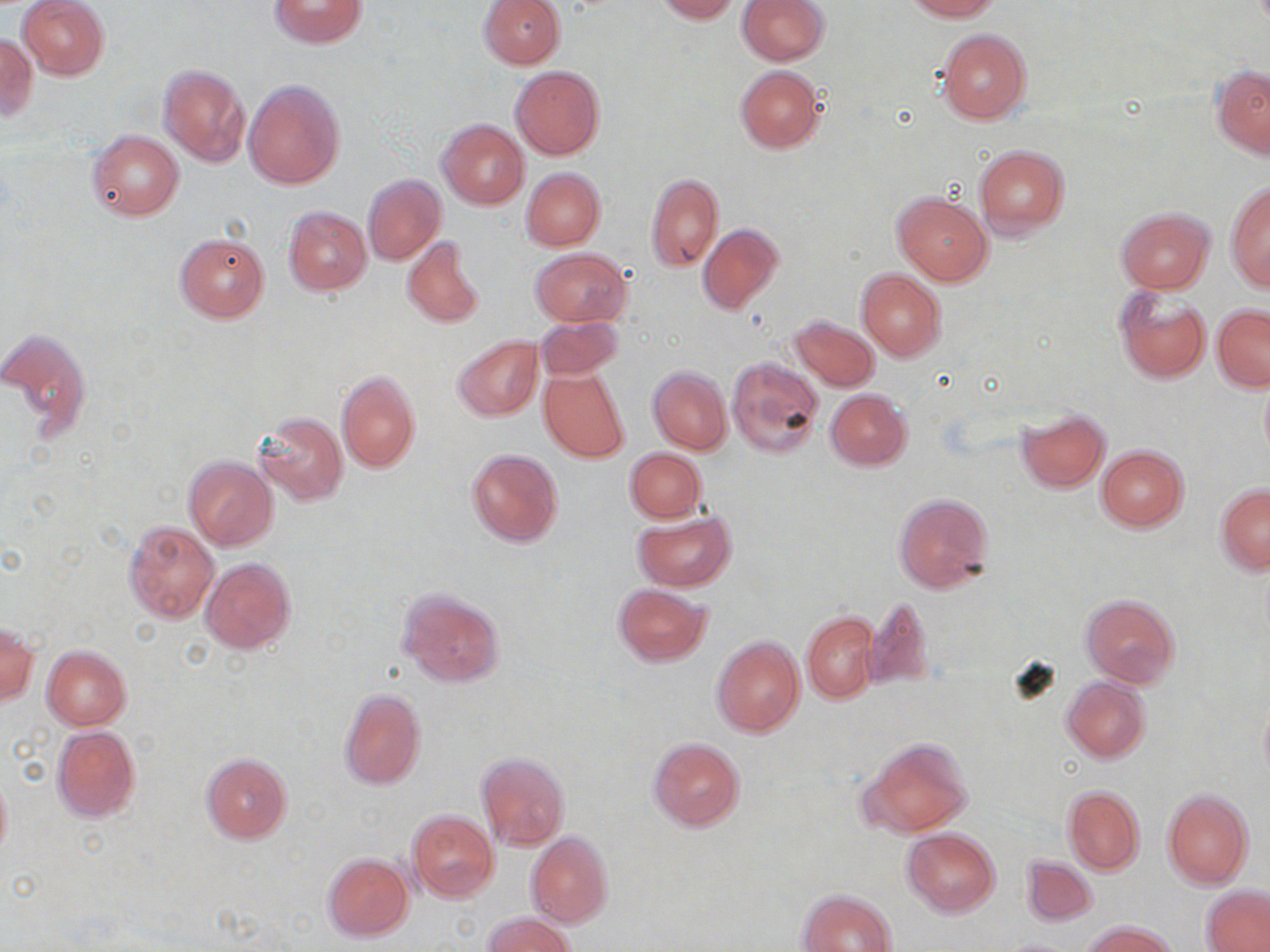 Approximate bounding boxes as named x1/y1/x2/y2 corners in pixels. Uninfected red blood cell locations: (x1=18, y1=0, x2=110, y2=80), (x1=268, y1=0, x2=367, y2=48), (x1=478, y1=0, x2=565, y2=69), (x1=654, y1=0, x2=738, y2=22), (x1=738, y1=0, x2=829, y2=65), (x1=905, y1=0, x2=1000, y2=21), (x1=936, y1=28, x2=1030, y2=123), (x1=0, y1=33, x2=38, y2=122), (x1=158, y1=65, x2=251, y2=166), (x1=735, y1=65, x2=825, y2=153), (x1=1213, y1=65, x2=1270, y2=159), (x1=511, y1=66, x2=604, y2=160), (x1=244, y1=79, x2=344, y2=189), (x1=438, y1=118, x2=529, y2=209), (x1=87, y1=130, x2=184, y2=221), (x1=973, y1=144, x2=1069, y2=238), (x1=521, y1=168, x2=605, y2=250), (x1=362, y1=174, x2=446, y2=266), (x1=646, y1=174, x2=724, y2=271), (x1=1225, y1=180, x2=1269, y2=291), (x1=893, y1=190, x2=993, y2=287), (x1=1116, y1=205, x2=1214, y2=293), (x1=283, y1=206, x2=372, y2=295), (x1=697, y1=223, x2=783, y2=315), (x1=175, y1=233, x2=269, y2=323), (x1=401, y1=236, x2=484, y2=330), (x1=531, y1=248, x2=631, y2=327), (x1=856, y1=270, x2=946, y2=360), (x1=1113, y1=286, x2=1211, y2=384), (x1=1211, y1=305, x2=1270, y2=392), (x1=788, y1=314, x2=879, y2=392), (x1=536, y1=315, x2=623, y2=379), (x1=0, y1=327, x2=92, y2=442), (x1=453, y1=335, x2=543, y2=422), (x1=726, y1=357, x2=825, y2=459), (x1=648, y1=366, x2=732, y2=454), (x1=539, y1=369, x2=629, y2=462), (x1=335, y1=370, x2=420, y2=473), (x1=825, y1=389, x2=912, y2=471), (x1=1016, y1=408, x2=1109, y2=492), (x1=255, y1=411, x2=348, y2=505), (x1=1096, y1=444, x2=1188, y2=532), (x1=466, y1=448, x2=564, y2=547), (x1=626, y1=448, x2=706, y2=522), (x1=184, y1=455, x2=278, y2=550), (x1=1215, y1=483, x2=1270, y2=574), (x1=893, y1=492, x2=994, y2=595), (x1=633, y1=511, x2=735, y2=592), (x1=125, y1=520, x2=218, y2=622), (x1=200, y1=557, x2=296, y2=655), (x1=612, y1=583, x2=712, y2=666), (x1=397, y1=588, x2=504, y2=687), (x1=1081, y1=593, x2=1180, y2=687), (x1=864, y1=598, x2=935, y2=691), (x1=802, y1=611, x2=879, y2=703), (x1=1, y1=625, x2=39, y2=708), (x1=712, y1=636, x2=805, y2=738), (x1=41, y1=645, x2=132, y2=730), (x1=1062, y1=676, x2=1150, y2=763), (x1=339, y1=687, x2=427, y2=791), (x1=1257, y1=691, x2=1270, y2=793), (x1=51, y1=725, x2=141, y2=822), (x1=858, y1=736, x2=973, y2=838), (x1=647, y1=737, x2=745, y2=831), (x1=201, y1=752, x2=292, y2=843), (x1=477, y1=753, x2=569, y2=851), (x1=0, y1=766, x2=12, y2=865), (x1=1062, y1=784, x2=1145, y2=876), (x1=1160, y1=788, x2=1253, y2=889), (x1=408, y1=809, x2=498, y2=901), (x1=902, y1=827, x2=1000, y2=916), (x1=525, y1=831, x2=613, y2=928), (x1=322, y1=853, x2=413, y2=941), (x1=1020, y1=855, x2=1098, y2=926), (x1=1202, y1=885, x2=1270, y2=951), (x1=799, y1=888, x2=896, y2=952), (x1=483, y1=912, x2=578, y2=952), (x1=1082, y1=920, x2=1178, y2=952). Slide-level diagnosis: negative for blood parasites. May-Grünwald-Giemsa-stained preparation. Image is 1270×952 pixels. Thin blood smear. Optical microscopy. One field of a larger specimen. 1000x magnification.